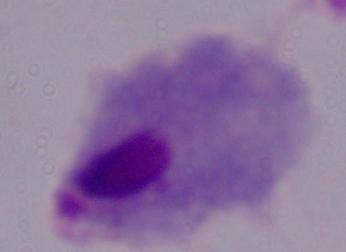 Captured at 1000x magnification. Photomicrograph. A trichomonad is seen.